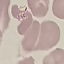
Result: negative for malaria parasites. Giemsa stain. Photographed with a smartphone camera at the microscope eyepiece. Automatically extracted cell patch, resized to 64 × 64 pixels. Thin blood film.